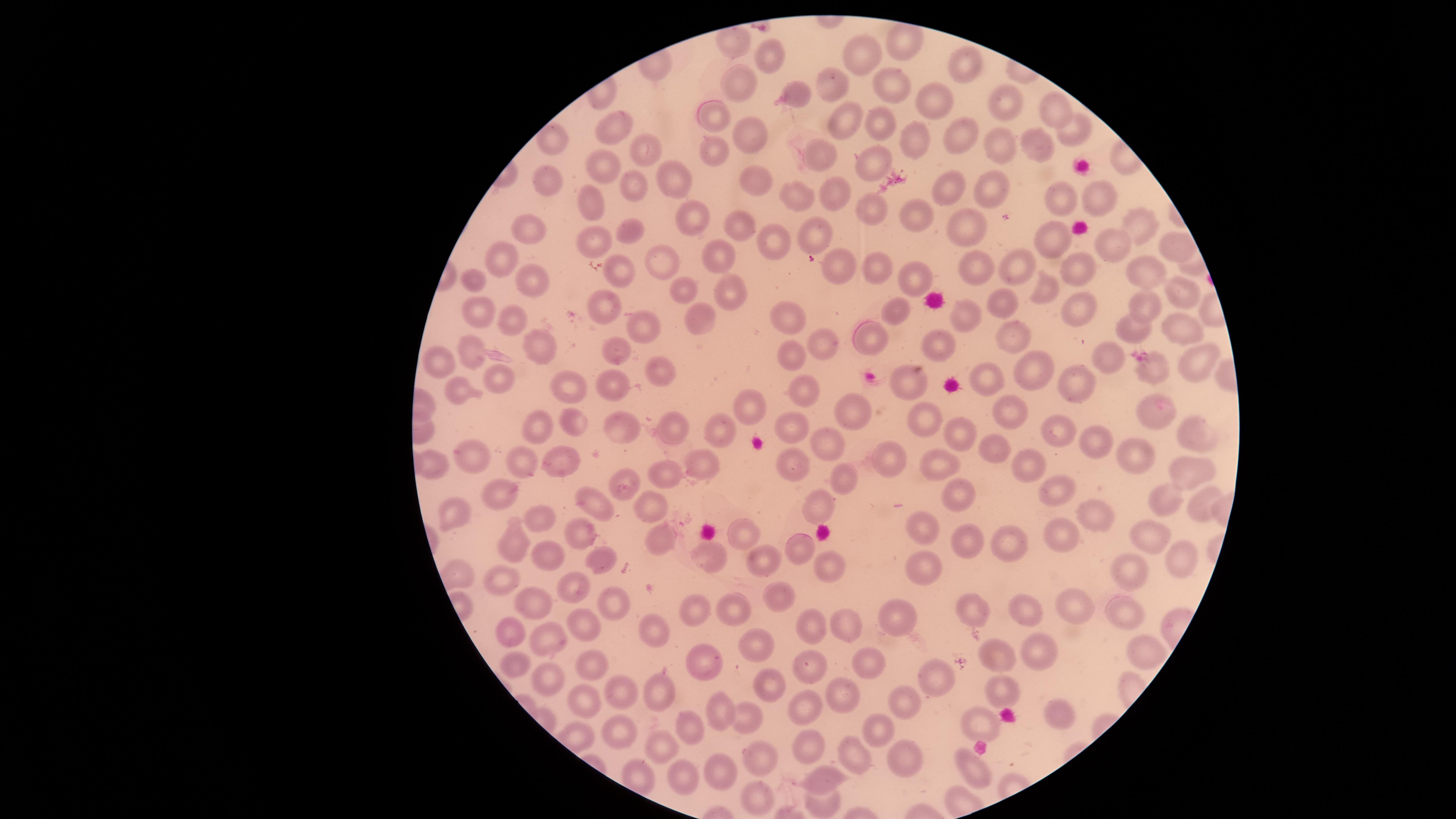

Approximate marker points as (x, y) in pixels.
Summary:
  - Uninfected RBCs: (903, 41), (736, 42), (766, 57), (863, 57), (968, 70), (740, 81), (836, 85), (892, 87), (797, 94), (1001, 103), (933, 106), (1051, 112), (715, 116), (835, 124), (880, 125), (616, 129), (1079, 131), (553, 135), (749, 142), (959, 143), (998, 143), (1044, 145), (913, 146), (641, 152), (715, 153), (817, 156), (870, 157), (602, 166), (541, 177), (675, 184), (634, 186), (761, 187), (989, 191), (826, 195), (948, 196), (583, 197), (795, 198), (1102, 199), (1061, 200), (874, 208), (920, 215), (740, 222), (961, 222), (691, 224), (1137, 225), (530, 226), (629, 233), (815, 234), (602, 241), (1057, 241), (777, 242), (1112, 245), (1178, 246), (716, 250), (505, 260), (655, 265), (614, 266), (845, 268), (876, 268), (1021, 270), (1077, 270), (975, 273), (909, 274), (1139, 274), (537, 284), (476, 286), (683, 290), (1177, 290), (720, 291), (1053, 293), (1002, 304), (604, 306), (1079, 307), (1149, 307), (896, 310), (474, 311), (783, 313), (968, 320), (504, 321), (695, 321), (1180, 327), (1131, 329), (645, 330), (867, 336), (1011, 337), (822, 342), (534, 345), (939, 345), (473, 352), (619, 353), (794, 356), (1105, 358), (1196, 358), (439, 360), (1151, 370), (1031, 372), (664, 373), (500, 379), (910, 381), (982, 381), (618, 382), (1074, 387), (459, 388), (565, 391), (806, 394), (757, 407), (859, 410), (1154, 413), (1009, 415), (931, 421), (793, 424), (673, 426), (576, 427), (615, 427), (539, 429), (1060, 429), (1183, 433), (723, 438), (967, 441), (825, 443), (1095, 444), (993, 452), (882, 456), (472, 458), (1138, 460), (565, 463), (706, 464), (794, 464), (437, 466), (520, 467), (1028, 467), (943, 468), (667, 476), (1200, 476), (845, 479), (625, 489), (1058, 490), (502, 491), (958, 493), (1159, 500), (593, 506), (648, 509), (823, 509), (1200, 509), (1091, 513), (544, 518), (457, 520), (924, 530), (740, 531), (1064, 533), (579, 535), (1008, 538), (655, 540), (1157, 541), (511, 545), (969, 545), (793, 549), (543, 556), (712, 556), (602, 557), (755, 559), (1180, 564), (828, 567), (921, 572), (1132, 575), (505, 584), (571, 590), (780, 599), (531, 603), (614, 607), (1074, 607), (700, 609), (739, 610), (975, 610), (1023, 614), (1120, 614), (896, 623), (809, 625), (585, 629), (838, 630), (515, 637), (549, 637), (652, 637), (758, 642), (1140, 649), (1039, 651), (993, 654), (862, 660), (596, 661), (817, 664), (709, 665), (522, 668), (545, 678), (934, 679), (766, 689), (1002, 689), (616, 691), (844, 693), (661, 694), (587, 699), (804, 701), (904, 703), (723, 707), (1054, 714), (748, 718), (983, 722), (614, 724), (687, 729), (870, 732), (665, 748), (802, 749), (756, 754), (857, 759), (901, 761), (970, 769), (720, 774), (829, 776), (686, 779), (754, 794), (826, 805)
  - Stain: Giemsa
  - Capture: smartphone photograph through the microscope eyepiece
  - Visible region: circular
  - Preparation: thin smear of blood
  - Image size: 1456×819 pixels
  - Field of view: single
  - Presence: no malaria parasites detected